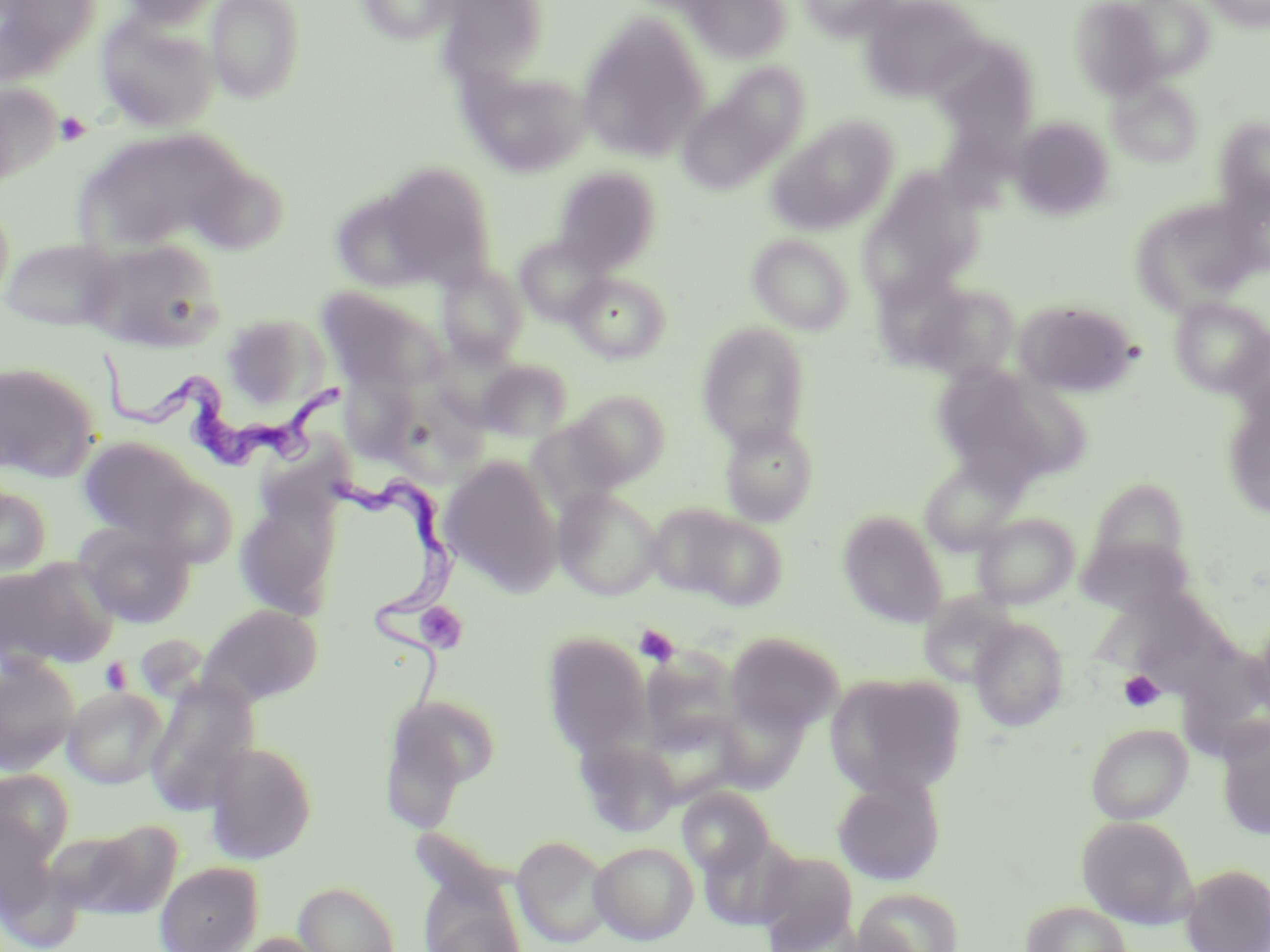
Summary:
  - Coordinate format: approximate bounding boxes as [x1, y1, x2, y2] in pixels
  - Uninfected red blood cell locations: [0, 0, 101, 77], [119, 0, 222, 28], [206, 0, 306, 103], [357, 0, 459, 45], [682, 0, 792, 63], [797, 0, 902, 40], [859, 0, 984, 102], [1068, 0, 1171, 99], [1202, 0, 1270, 31], [440, 1, 551, 78], [1113, 1, 1216, 83], [96, 13, 220, 132], [578, 14, 710, 161], [930, 36, 1039, 153], [466, 68, 592, 176], [678, 70, 806, 193], [1108, 78, 1204, 167], [0, 80, 62, 185], [768, 116, 900, 235], [1009, 117, 1116, 220], [1214, 117, 1270, 218], [78, 127, 254, 256], [376, 162, 498, 287], [553, 167, 662, 274], [859, 171, 984, 301], [329, 190, 441, 295], [0, 195, 15, 306], [1130, 197, 1262, 315], [747, 233, 855, 335], [514, 235, 611, 325], [2, 237, 124, 331], [79, 238, 222, 351], [437, 263, 528, 366], [567, 273, 671, 363], [913, 281, 1020, 382], [316, 286, 447, 394], [1170, 297, 1270, 397], [1014, 299, 1139, 397], [219, 312, 330, 413], [697, 322, 811, 450], [474, 359, 573, 442], [0, 360, 101, 481], [933, 363, 1083, 492], [340, 372, 421, 464], [568, 390, 671, 487], [922, 390, 1057, 550], [1223, 396, 1270, 518], [525, 420, 627, 516], [719, 420, 818, 526], [77, 436, 200, 541], [439, 456, 562, 595], [918, 457, 1025, 555], [0, 484, 53, 579], [554, 487, 662, 599], [233, 498, 339, 620], [645, 502, 747, 598], [838, 510, 948, 628], [672, 511, 788, 610], [973, 512, 1080, 609], [76, 522, 196, 628], [1075, 534, 1196, 618], [0, 557, 118, 671], [918, 591, 1019, 688], [1106, 594, 1230, 696], [200, 604, 323, 705], [970, 618, 1070, 732], [1249, 618, 1270, 726], [724, 631, 843, 737], [542, 633, 652, 759], [0, 654, 81, 776], [825, 672, 967, 797], [144, 674, 259, 812], [63, 685, 169, 788], [384, 693, 501, 799], [640, 713, 746, 807], [1086, 723, 1192, 824], [1217, 723, 1270, 840], [574, 735, 682, 836], [205, 740, 318, 864], [1, 770, 73, 881], [832, 773, 945, 886], [677, 787, 774, 878], [1078, 815, 1198, 929], [74, 820, 182, 919], [511, 835, 611, 948], [589, 841, 699, 944], [755, 849, 858, 950], [155, 861, 263, 952], [1180, 863, 1269, 952], [418, 879, 528, 952], [293, 881, 400, 952], [854, 887, 963, 952], [1021, 900, 1131, 952], [231, 931, 336, 952]
  - Trypanosoma brucei locations: [91, 348, 345, 471], [325, 467, 466, 711]
  - Platelet locations: [55, 111, 92, 146], [413, 603, 469, 655], [633, 624, 681, 666], [101, 658, 133, 695], [1119, 670, 1165, 712]
  - Slide-level diagnosis: Trypanosoma brucei
  - Field of view: single
  - Preparation: thin blood film
  - Magnification: 1000x
  - Modality: light microscopy
  - Stain: May-Grünwald-Giemsa
  - Image size: 1270×952 pixels